Describe the morphology of the erythrocytes.
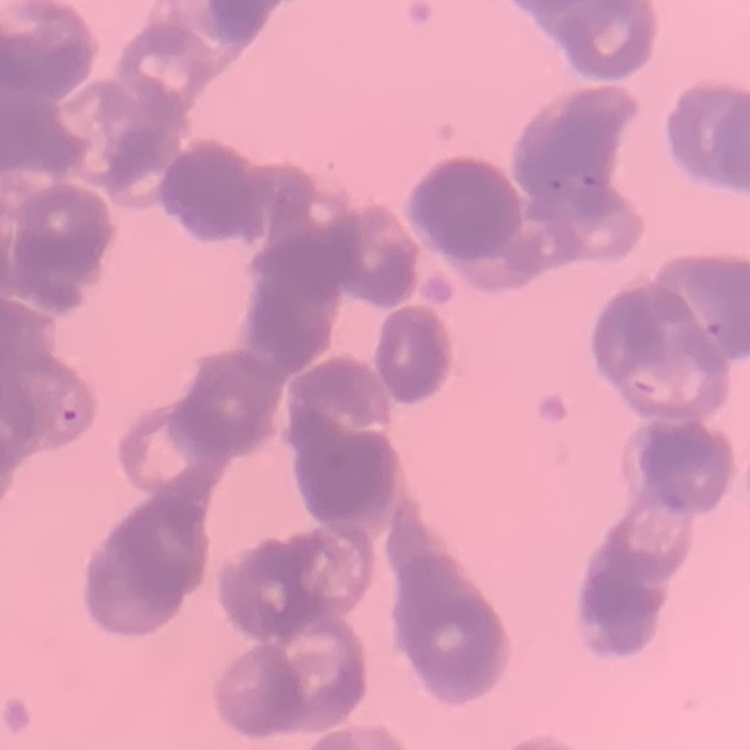
Rouleaux formation.

preparation: thin blood film
stain: Field's or Giemsa
image_type: square crop of a larger photomicrograph